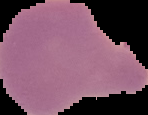 From a thin blood smear. Result: Plasmodium parasites identified. Image is 148×115 pixels. Cell region segmented out of the field of view; the surrounding area is masked to black.